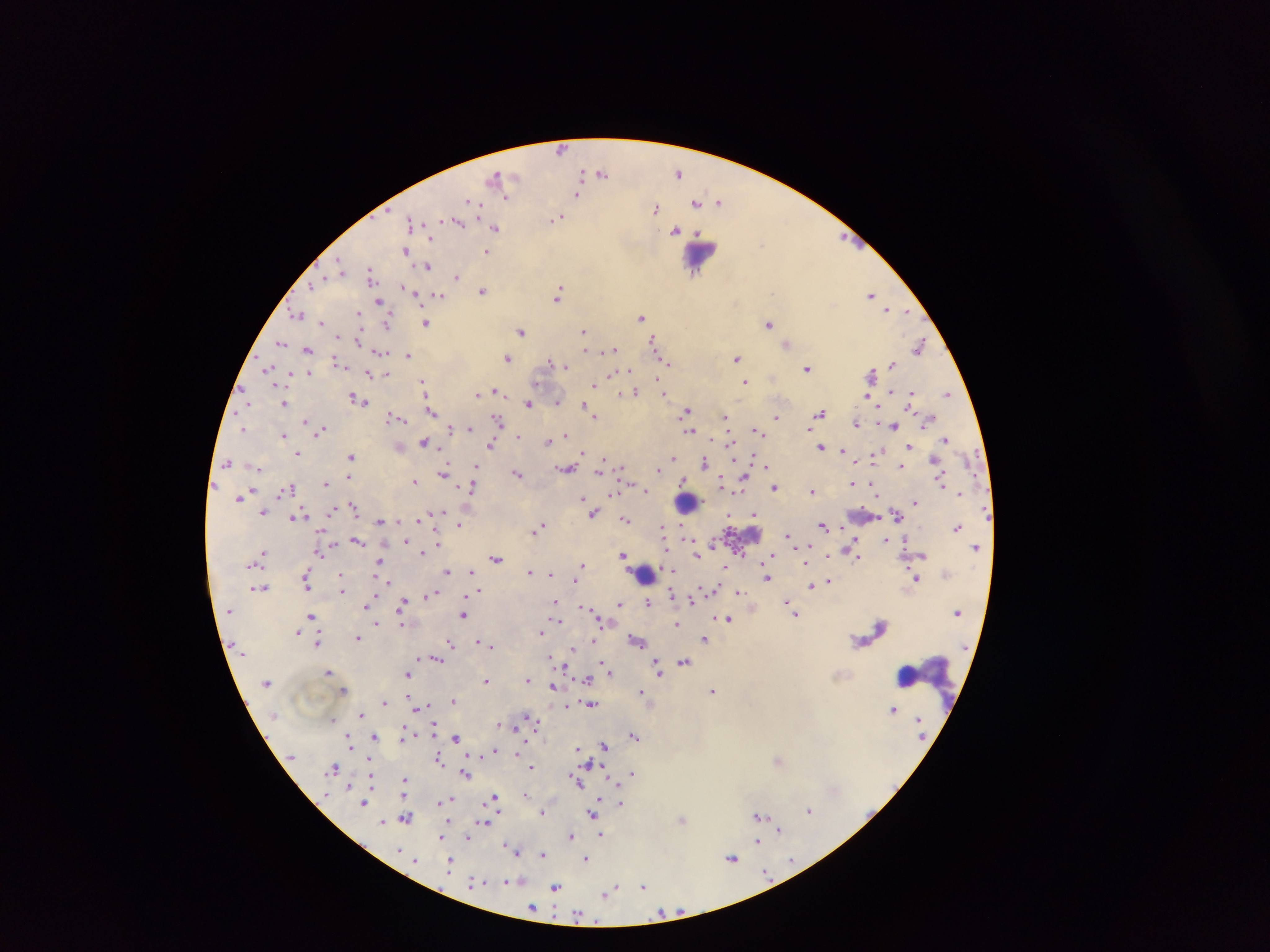
Approximate centers as x y in pixels. Plasmodium parasite locations: 563 149; 601 172; 678 172; 581 174; 497 175; 578 194; 507 197; 472 202; 696 202; 719 203; 655 208; 556 219; 411 221; 457 221; 495 227; 676 230; 431 238; 762 243; 406 250; 486 251; 341 266; 428 266; 371 272; 457 277; 311 285; 406 288; 483 290; 411 291; 558 294; 440 295; 871 295; 378 301; 887 310; 297 314; 359 315; 642 317; 321 323; 387 323; 426 323; 768 323; 583 330; 522 332; 358 340; 653 340; 281 342; 787 343; 919 346; 307 349; 585 350; 612 350; 380 352; 408 355; 736 357; 507 358; 550 361; 666 362; 337 363; 892 364; 565 367; 807 368; 267 369; 629 371; 370 374; 385 374; 611 374; 871 374; 659 381; 423 382; 745 382; 594 385; 496 391; 626 392; 636 392; 664 393; 946 393; 478 394; 911 394; 867 396; 356 398; 362 401; 557 401; 284 403; 529 403; 584 406; 590 408; 432 411; 686 411; 821 413; 595 416; 397 418; 776 418; 726 419; 498 420; 306 422; 856 424; 893 426; 470 428; 243 429; 452 429; 322 430; 690 430; 757 430; 283 435; 518 435; 566 435; 946 438; 547 441; 729 441; 424 442; 492 445; 909 446; 822 447; 843 451; 582 453; 298 454; 350 456; 874 457; 604 458; 673 458; 752 458; 705 461; 227 463; 766 466; 901 466; 476 467; 621 469; 659 469; 566 470; 600 471; 444 472; 517 474; 683 480; 414 481; 941 481; 721 482; 744 482; 853 483; 326 484; 872 485; 472 487; 290 488; 740 488; 774 488; 645 490; 812 490; 960 492; 614 493; 240 496; 582 497; 915 502; 355 508; 263 512; 593 513; 753 514; 897 515; 294 517; 419 519; 625 520; 380 521; 459 524; 823 525; 539 527; 958 527; 663 530; 789 536; 885 539; 357 541; 712 544; 320 551; 853 552; 264 553; 423 553; 623 554; 696 554; 773 556; 496 558; 806 561; 381 562; 582 566; 580 569; 723 569; 447 571; 471 571; 530 572; 549 574; 341 576; 767 578; 916 578; 305 581; 828 581; 386 582; 823 583; 342 584; 811 585; 260 588; 342 589; 713 590; 477 591; 739 592; 432 594; 672 595; 694 597; 691 601; 403 602; 554 602; 648 602; 787 602; 619 604; 366 606; 585 608; 310 615; 463 615; 795 615; 727 619; 677 624; 298 632; 541 632; 358 638; 705 639; 593 640; 479 641; 637 641; 318 642; 450 643; 490 644; 572 648; 550 657; 435 659; 602 662; 684 663; 605 665; 658 667; 608 670; 328 672; 408 674; 527 679; 587 679; 486 680; 553 687; 344 690; 642 691; 713 692; 453 700; 384 702; 591 705; 421 706; 567 706; 893 709; 361 715; 333 720; 537 721; 515 727; 634 736; 374 737; 456 738; 605 745; 578 749; 493 750; 517 752; 438 760; 778 760; 588 763; 333 768; 531 768; 633 773; 466 775; 404 780; 576 780; 526 794; 493 798; 449 800; 444 802; 364 803; 620 804; 809 810; 542 811; 592 815; 758 815; 406 817; 682 820; 383 823; 483 823; 779 829; 601 835; 571 836; 441 837; 467 839; 756 842; 515 850; 542 854; 732 858; 586 860; 791 861; 449 864; 766 871; 519 880; 475 882; 510 882; 643 886; 555 887; 610 891; 532 908; 661 913; 579 914. Leukocyte locations: 698 254; 688 501; 644 574; 909 678. Thick blood film. One field of view. Mobile-phone photograph taken through the microscope. Sample from Ghana. Image is 1270×952 pixels.